Describe the morphology of the red blood cells.
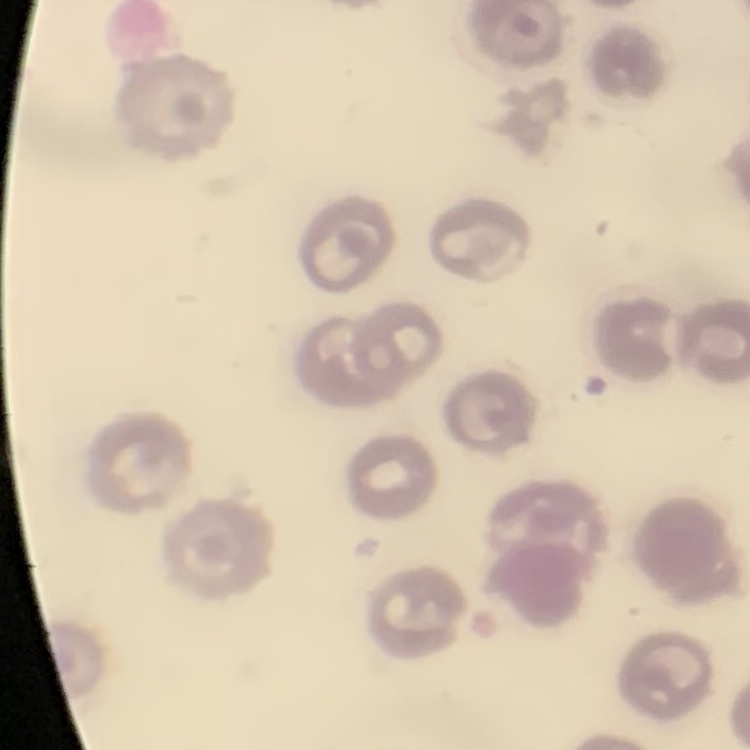

No rouleaux formation.

{
  "stain": "Field's or Giemsa",
  "image_type": "one tile cut from a larger photomicrograph",
  "preparation": "thin blood smear"
}